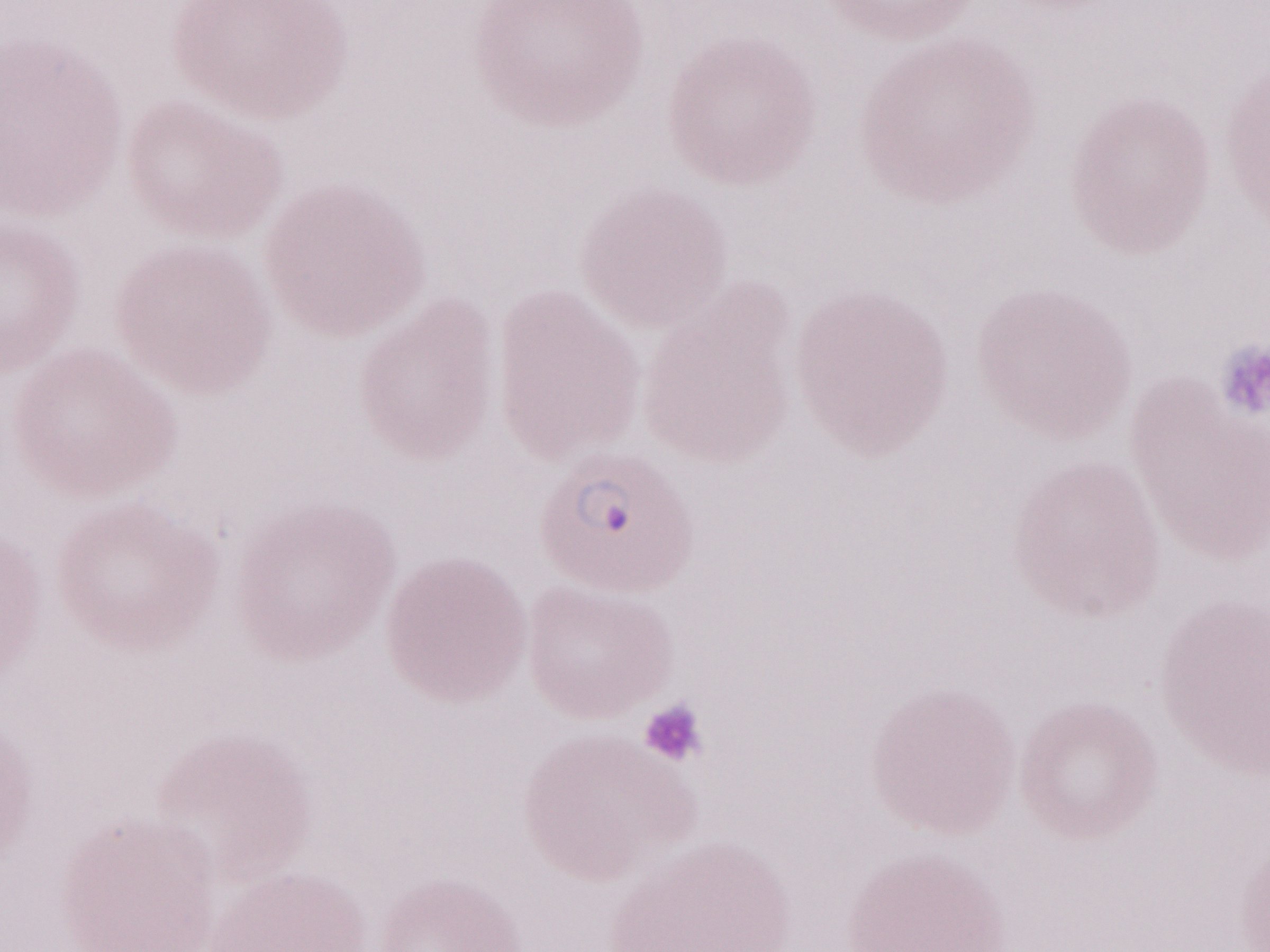
Malaria diagnosis (patient-level): positive. May-Grünwald-Giemsa (MGG) stain. Olympus BX43 microscope and DP73 digital camera. Image is 1270×952 pixels. Thin blood film. One field of this slide. Magnification: 1,000x.